Outline each blood parasite and name the species.
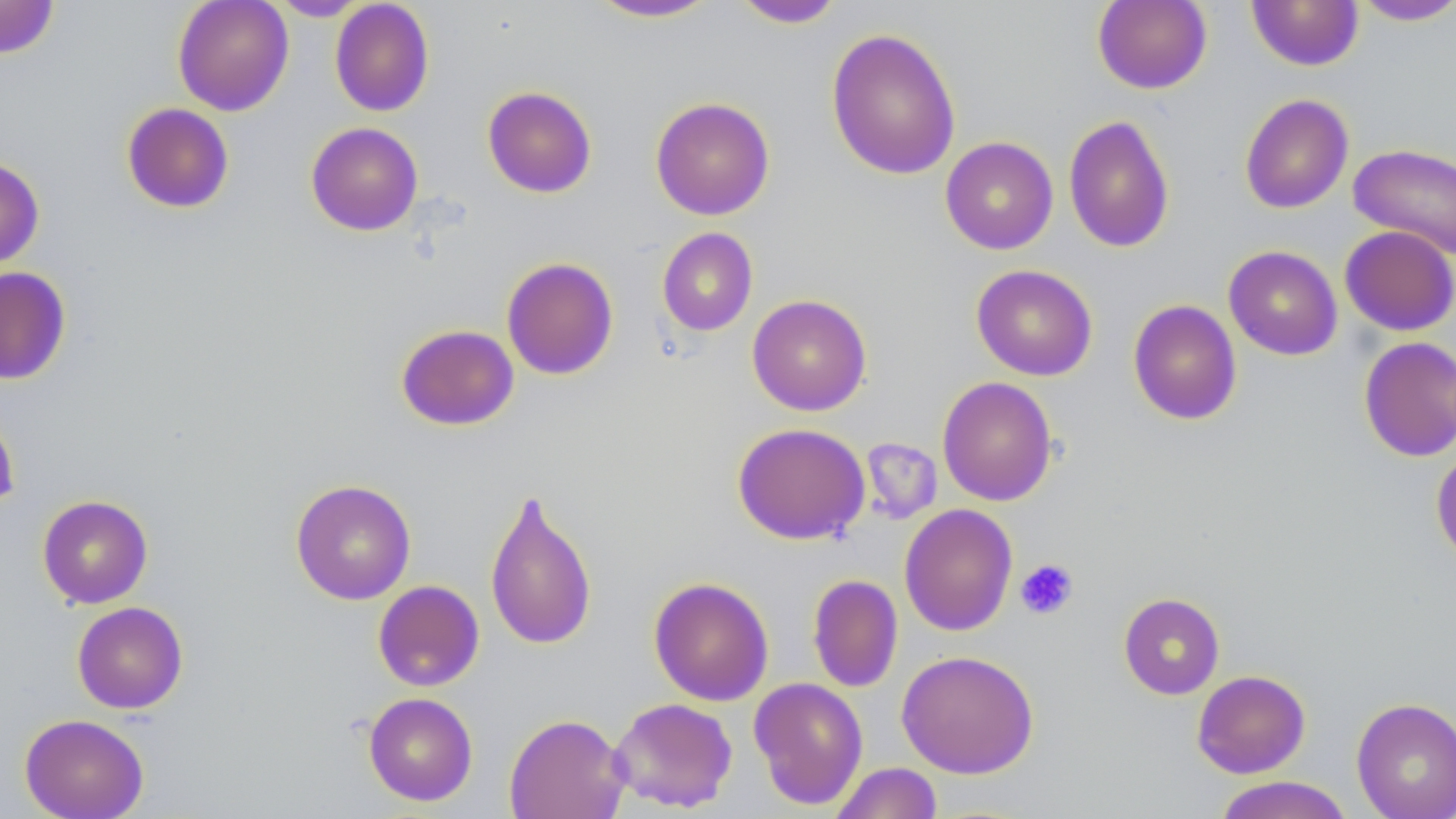
No blood parasites seen.

Summary:
  - Coordinate format: approximate bounding boxes as (x1, y1, x2, y2) in pixels
  - Platelet locations: (1015, 558, 1079, 620)
  - Uninfected red blood cell locations: (0, 0, 59, 59), (172, 0, 294, 116), (268, 0, 371, 21), (585, 0, 724, 23), (731, 0, 846, 28), (1092, 0, 1212, 94), (330, 1, 434, 117), (1247, 1, 1364, 71), (1349, 1, 1456, 27), (825, 27, 961, 181), (482, 85, 597, 198), (1239, 93, 1354, 214), (650, 96, 775, 220), (121, 103, 235, 214), (1063, 114, 1175, 254), (305, 122, 423, 235), (940, 137, 1058, 254), (1348, 143, 1456, 259), (0, 156, 45, 269), (1339, 225, 1456, 336), (656, 227, 758, 336), (1223, 245, 1343, 360), (501, 257, 619, 380), (970, 264, 1098, 381), (0, 266, 72, 384), (747, 294, 872, 416), (1128, 299, 1243, 426), (395, 324, 520, 431), (1358, 336, 1456, 462), (937, 376, 1058, 506), (0, 406, 20, 515), (732, 422, 870, 545), (1431, 445, 1456, 568), (290, 479, 416, 605), (484, 487, 598, 651), (37, 494, 153, 609), (899, 503, 1018, 636), (807, 574, 903, 693), (648, 576, 774, 706), (372, 580, 484, 691), (1118, 593, 1225, 699), (72, 601, 188, 714), (896, 650, 1040, 778), (1192, 670, 1311, 778), (749, 677, 869, 810), (363, 692, 478, 806), (1351, 696, 1456, 819), (608, 697, 739, 813), (19, 713, 149, 819), (504, 713, 630, 819), (829, 762, 943, 819), (1212, 775, 1355, 819)
  - Slide-level diagnosis: no evidence of blood parasites
  - Stain: May-Grünwald-Giemsa
  - Image size: 1456×819 pixels
  - Field of view: one of a larger specimen
  - Modality: optical microscopy
  - Magnification: 1000x
  - Preparation: thin blood film